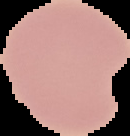

image size = 130×136 pixels
preparation = thin blood film
malaria status = uninfected
image type = cell region segmented out of the field of view; surrounding area masked to black